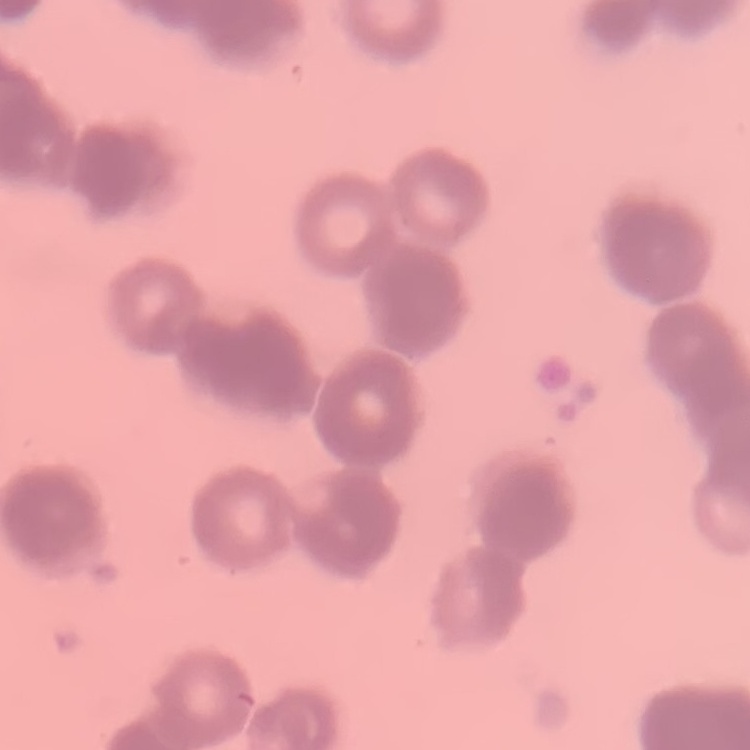
red blood cell morphology = rouleaux formation
stain = Field's or Giemsa
image type = one tile cut from a larger photomicrograph
preparation = thin peripheral smear